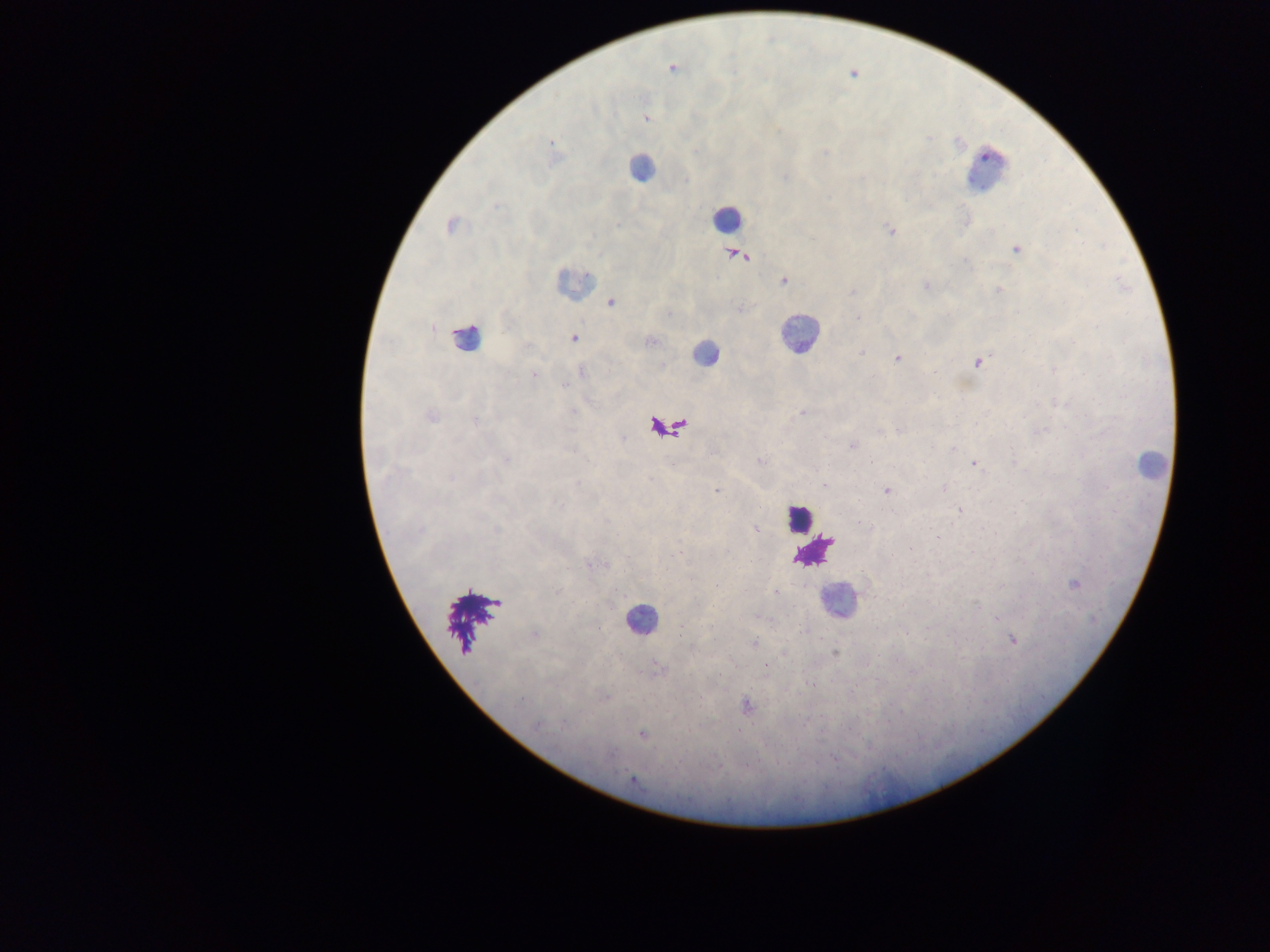

capture = mobile-phone photograph through a microscope
malaria parasite locations = approximate centers as [x, y] in pixels: [672, 68], [646, 119], [551, 143], [696, 150], [785, 177], [450, 225], [890, 230], [1017, 250], [738, 255], [784, 281], [925, 285], [998, 290], [853, 292], [611, 303], [858, 318], [574, 339], [650, 341], [861, 352], [898, 358], [978, 363], [934, 371], [582, 372], [533, 375], [563, 386], [802, 413], [431, 416], [476, 422], [899, 430], [851, 445], [954, 448], [760, 461], [871, 461], [973, 463], [650, 478], [824, 485], [944, 488], [716, 491], [887, 491], [959, 510], [982, 528], [756, 530], [495, 531], [938, 536], [680, 552], [589, 565], [1074, 585], [716, 586], [776, 592], [758, 618], [997, 618], [801, 632], [535, 634], [1013, 640], [753, 643], [835, 653], [765, 666], [658, 667], [521, 700], [746, 706], [807, 721], [564, 724], [538, 725], [642, 735], [632, 780]
field of view = single
preparation = thick blood smear
leukocyte locations = approximate centers as [x, y] in pixels: [641, 168], [988, 169], [727, 218], [577, 282], [798, 334], [467, 337], [705, 353], [1151, 463], [798, 518], [811, 551], [837, 600], [640, 619]
image size = 1270×952 pixels
country = Ghana